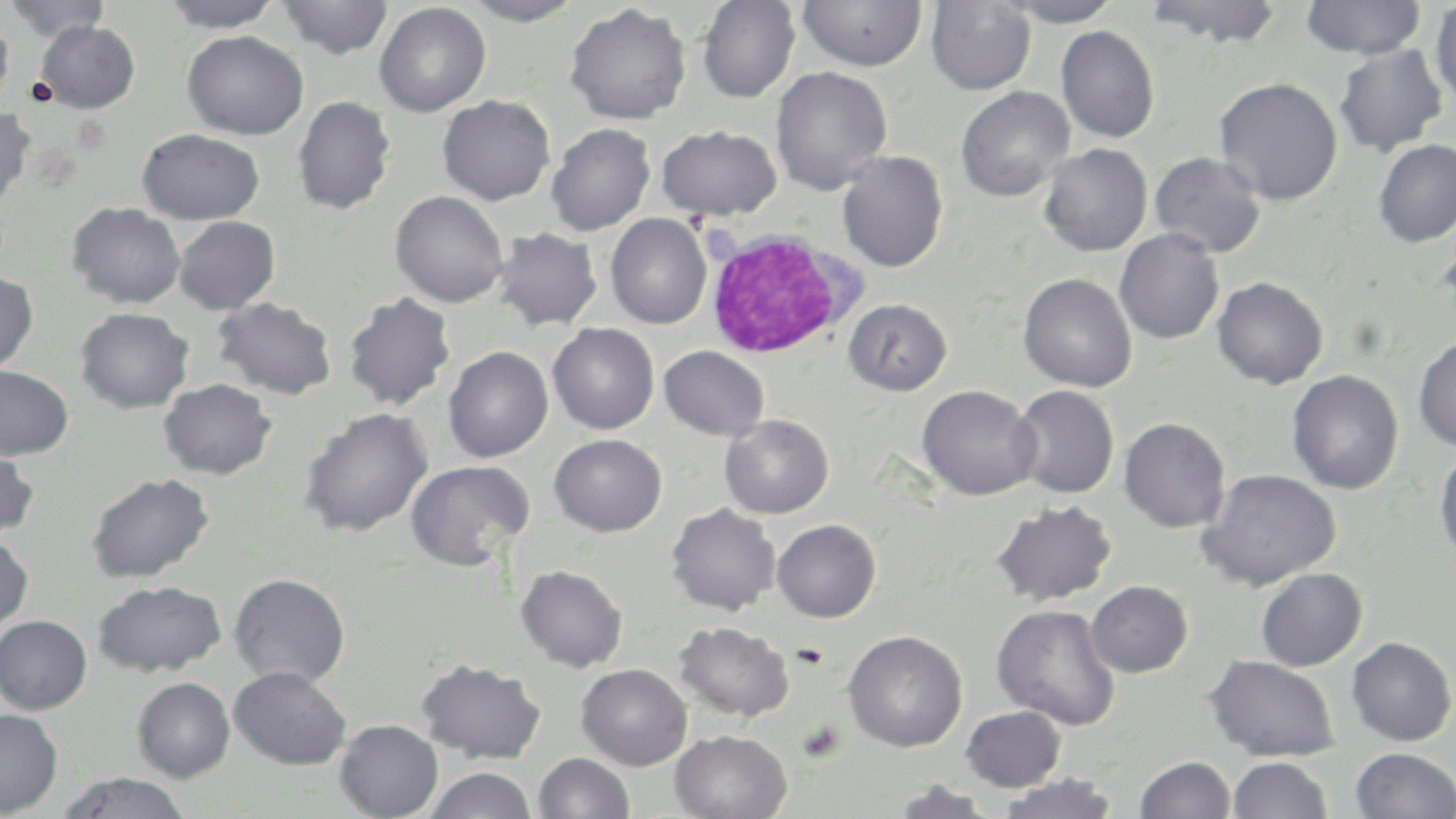
Summary:
  - Coordinate format: approximate bounding boxes as [x1, y1, x2, y2] in pixels
  - White blood cell locations: [704, 228, 861, 360]
  - Uninfected red blood cell locations: [4, 0, 111, 43], [161, 0, 283, 32], [276, 0, 394, 59], [461, 0, 586, 25], [697, 0, 800, 102], [796, 0, 927, 71], [1001, 0, 1123, 26], [1302, 0, 1425, 59], [926, 1, 1037, 95], [1145, 1, 1285, 49], [1431, 2, 1456, 110], [374, 3, 491, 116], [565, 3, 691, 124], [0, 16, 14, 104], [34, 20, 140, 112], [1056, 26, 1159, 143], [182, 30, 309, 139], [1333, 44, 1448, 157], [770, 66, 892, 195], [1214, 77, 1343, 205], [955, 86, 1074, 201], [437, 94, 555, 205], [292, 95, 395, 215], [0, 105, 35, 211], [546, 123, 656, 235], [656, 124, 781, 220], [137, 128, 264, 223], [1373, 139, 1456, 247], [1039, 143, 1153, 256], [837, 150, 948, 272], [1149, 151, 1267, 258], [390, 190, 509, 307], [67, 202, 186, 308], [605, 213, 712, 329], [174, 216, 281, 314], [493, 227, 603, 331], [1114, 228, 1224, 344], [1436, 236, 1456, 325], [0, 270, 38, 375], [1018, 273, 1137, 392], [1212, 276, 1328, 389], [343, 292, 456, 411], [212, 297, 337, 399], [844, 298, 952, 395], [75, 307, 194, 413], [547, 323, 660, 434], [1413, 335, 1456, 451], [659, 345, 769, 440], [443, 346, 553, 462], [0, 365, 74, 459], [1286, 369, 1403, 494], [158, 378, 277, 479], [918, 384, 1040, 500], [1011, 385, 1119, 499], [298, 407, 433, 536], [720, 415, 834, 518], [1119, 417, 1231, 533], [549, 433, 667, 536], [1433, 445, 1456, 563], [0, 446, 39, 542], [405, 460, 534, 570], [1197, 468, 1341, 591], [86, 472, 214, 582], [992, 499, 1117, 606], [666, 504, 781, 615], [772, 519, 881, 622], [0, 536, 33, 633], [516, 565, 628, 671], [1255, 567, 1367, 671], [229, 572, 350, 687], [93, 579, 226, 677], [1086, 581, 1193, 677], [991, 603, 1122, 730], [0, 615, 93, 714], [674, 620, 794, 721], [843, 630, 967, 752], [1346, 636, 1455, 745], [1205, 654, 1340, 761], [416, 658, 546, 763], [576, 663, 692, 769], [229, 665, 352, 769], [132, 677, 235, 782], [961, 706, 1066, 791], [0, 709, 63, 816], [335, 719, 443, 819], [671, 729, 792, 819], [1351, 748, 1456, 818], [534, 752, 635, 818], [1135, 755, 1235, 818], [1227, 756, 1333, 818], [424, 767, 537, 819], [56, 772, 193, 818], [996, 772, 1119, 819], [886, 780, 999, 819]
  - Platelet locations: [797, 720, 845, 763]
  - Slide-level diagnosis: no evidence of blood parasites
  - Image size: 1456×819 pixels
  - Stain: May-Grünwald-Giemsa
  - Field of view: single
  - Magnification: 1000x
  - Modality: light microscopy
  - Preparation: thin blood smear